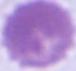 Photomicrograph. Captured at 1000x magnification. A red blood cell is seen.